Assess this cell for malaria.
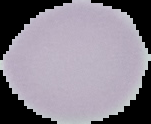
Uninfected.

image size = 151×124 pixels
image type = cell region segmented out of the field of view; surrounding area masked to black
preparation = thin blood smear